State which parasite is depicted.
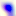
This is Toxoplasma gondii.

magnification = 400x
modality = photomicrograph